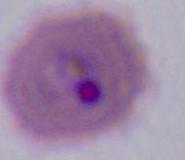
Photomicrograph. A Plasmodium parasite is seen. 400x or 1000x magnification.